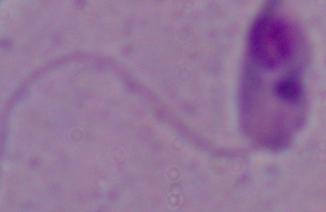

1000x magnification. A Leishmania parasite is seen. Micrograph.